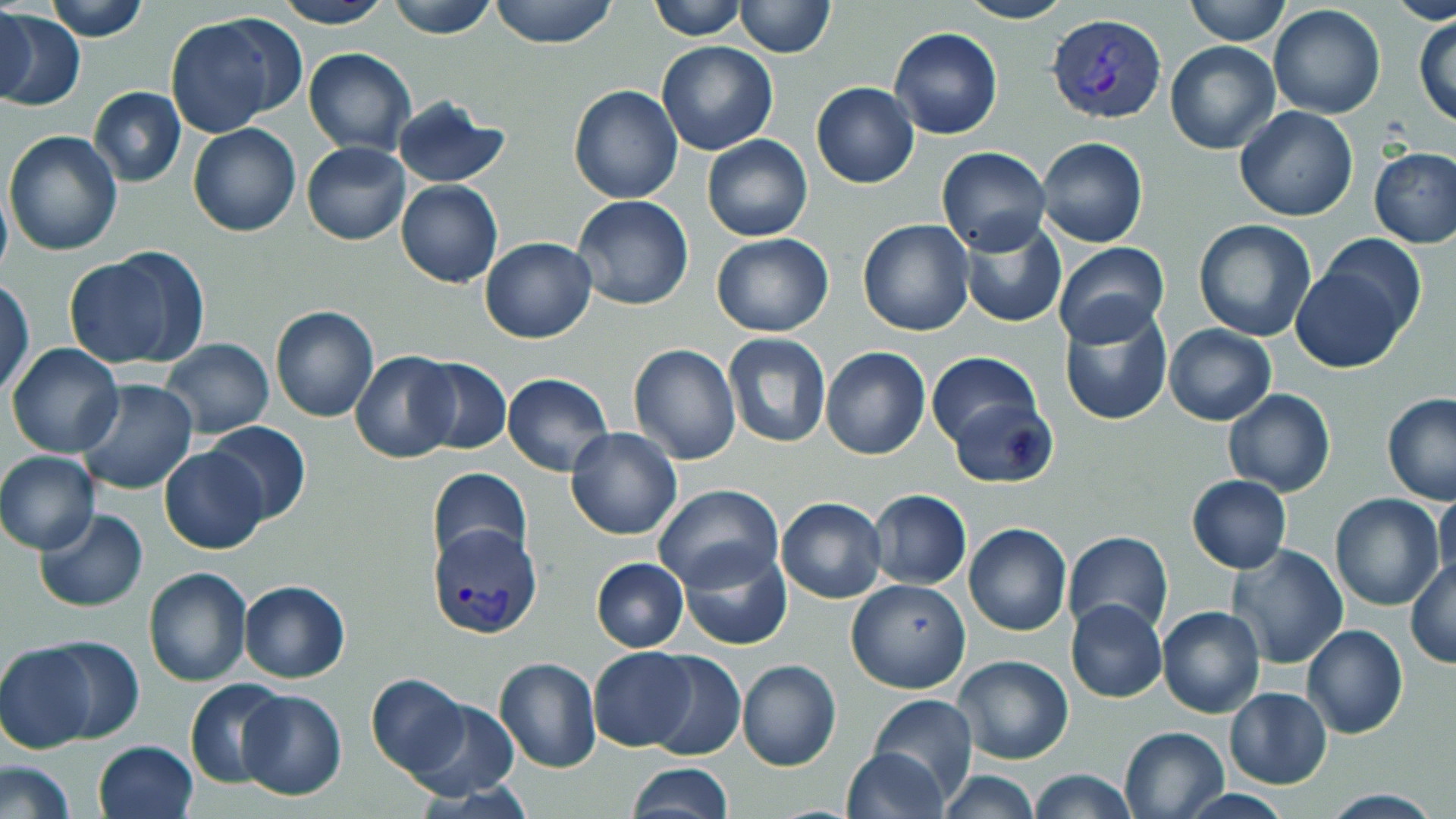

slide-level diagnosis = Plasmodium vivax
modality = optical microscopy
stain = May-Grünwald-Giemsa
magnification = 1000x
field of view = single
preparation = thin blood smear
uninfected red blood cell locations = approximate bounding boxes as named x1/y1/x2/y2 corners in pixels: (x1=43, y1=0, x2=148, y2=41), (x1=273, y1=0, x2=393, y2=28), (x1=387, y1=0, x2=498, y2=39), (x1=490, y1=0, x2=618, y2=48), (x1=646, y1=0, x2=746, y2=40), (x1=733, y1=0, x2=836, y2=57), (x1=954, y1=0, x2=1076, y2=24), (x1=1185, y1=0, x2=1289, y2=45), (x1=1388, y1=1, x2=1456, y2=25), (x1=1268, y1=2, x2=1386, y2=120), (x1=0, y1=4, x2=35, y2=106), (x1=0, y1=8, x2=84, y2=113), (x1=163, y1=13, x2=297, y2=138), (x1=1414, y1=13, x2=1456, y2=127), (x1=888, y1=26, x2=1004, y2=139), (x1=656, y1=40, x2=778, y2=156), (x1=1165, y1=40, x2=1281, y2=154), (x1=303, y1=48, x2=417, y2=155), (x1=810, y1=82, x2=920, y2=189), (x1=568, y1=84, x2=682, y2=205), (x1=87, y1=87, x2=186, y2=187), (x1=390, y1=94, x2=510, y2=188), (x1=1234, y1=106, x2=1359, y2=220), (x1=187, y1=122, x2=301, y2=237), (x1=3, y1=130, x2=124, y2=256), (x1=702, y1=134, x2=812, y2=242), (x1=1036, y1=136, x2=1148, y2=248), (x1=303, y1=142, x2=412, y2=245), (x1=936, y1=146, x2=1050, y2=256), (x1=1370, y1=146, x2=1456, y2=249), (x1=396, y1=180, x2=503, y2=288), (x1=0, y1=181, x2=12, y2=286), (x1=572, y1=195, x2=693, y2=311), (x1=958, y1=218, x2=1068, y2=328), (x1=1194, y1=218, x2=1317, y2=342), (x1=858, y1=219, x2=974, y2=336), (x1=712, y1=234, x2=834, y2=336), (x1=1318, y1=234, x2=1425, y2=340), (x1=480, y1=237, x2=597, y2=343), (x1=1052, y1=241, x2=1170, y2=350), (x1=67, y1=249, x2=207, y2=372), (x1=1290, y1=266, x2=1410, y2=373), (x1=0, y1=279, x2=35, y2=400), (x1=270, y1=305, x2=378, y2=422), (x1=1058, y1=305, x2=1173, y2=428), (x1=1164, y1=323, x2=1276, y2=424), (x1=721, y1=333, x2=832, y2=450), (x1=160, y1=338, x2=274, y2=438), (x1=6, y1=342, x2=123, y2=459), (x1=627, y1=344, x2=740, y2=464), (x1=821, y1=347, x2=931, y2=460), (x1=350, y1=351, x2=462, y2=463), (x1=927, y1=352, x2=1043, y2=452), (x1=413, y1=358, x2=511, y2=455), (x1=502, y1=372, x2=613, y2=476), (x1=76, y1=378, x2=197, y2=495), (x1=1223, y1=388, x2=1336, y2=496), (x1=1382, y1=392, x2=1456, y2=505), (x1=945, y1=393, x2=1057, y2=490), (x1=203, y1=420, x2=311, y2=525), (x1=566, y1=428, x2=683, y2=541), (x1=159, y1=446, x2=269, y2=555), (x1=1, y1=450, x2=100, y2=553), (x1=427, y1=468, x2=530, y2=567), (x1=1187, y1=475, x2=1291, y2=573), (x1=652, y1=484, x2=784, y2=592), (x1=868, y1=490, x2=972, y2=589), (x1=1434, y1=490, x2=1456, y2=588), (x1=1330, y1=493, x2=1445, y2=610), (x1=775, y1=497, x2=887, y2=604), (x1=34, y1=509, x2=149, y2=612), (x1=964, y1=523, x2=1071, y2=635), (x1=1064, y1=531, x2=1174, y2=640), (x1=678, y1=541, x2=793, y2=652), (x1=1227, y1=544, x2=1348, y2=669), (x1=591, y1=558, x2=689, y2=651), (x1=1406, y1=558, x2=1455, y2=669), (x1=143, y1=567, x2=251, y2=686), (x1=846, y1=577, x2=972, y2=693), (x1=238, y1=579, x2=350, y2=684), (x1=1066, y1=598, x2=1166, y2=703), (x1=1157, y1=604, x2=1266, y2=718), (x1=1302, y1=625, x2=1407, y2=740), (x1=39, y1=635, x2=144, y2=744), (x1=0, y1=641, x2=99, y2=753), (x1=588, y1=648, x2=697, y2=751), (x1=643, y1=650, x2=746, y2=760), (x1=950, y1=655, x2=1074, y2=765), (x1=494, y1=656, x2=602, y2=773), (x1=736, y1=659, x2=841, y2=772), (x1=366, y1=673, x2=470, y2=776), (x1=186, y1=678, x2=290, y2=788), (x1=1224, y1=688, x2=1332, y2=790), (x1=237, y1=690, x2=347, y2=800), (x1=869, y1=694, x2=977, y2=803), (x1=404, y1=696, x2=521, y2=801), (x1=1117, y1=725, x2=1231, y2=818), (x1=93, y1=739, x2=198, y2=819), (x1=842, y1=747, x2=949, y2=819), (x1=0, y1=757, x2=77, y2=819), (x1=626, y1=763, x2=732, y2=819), (x1=1025, y1=768, x2=1136, y2=819), (x1=935, y1=770, x2=1043, y2=819)
image size = 1456×819 pixels
Plasmodium vivax-infected red blood cell locations = approximate bounding boxes as named x1/y1/x2/y2 corners in pixels: (x1=1047, y1=15, x2=1166, y2=123), (x1=428, y1=519, x2=542, y2=639)